Report the malaria status of this cell.
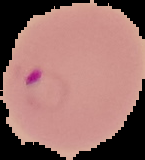
It is parasitized.

Summary:
  - Image type: cell region segmented out of the field of view; surrounding area masked to black
  - Image size: 145×160 pixels
  - Preparation: thin blood smear